Comment on the morphology of the red blood cells.
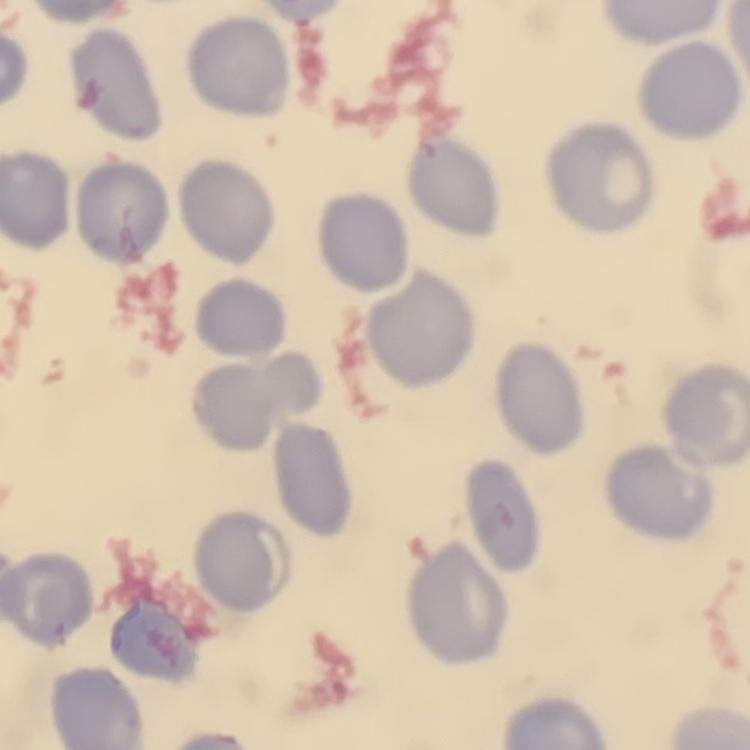

They show no rouleaux formation.

preparation: thin blood smear
stain: Field's or Giemsa
image_type: square crop of a larger photomicrograph